Locate every blood parasite and identify its species.
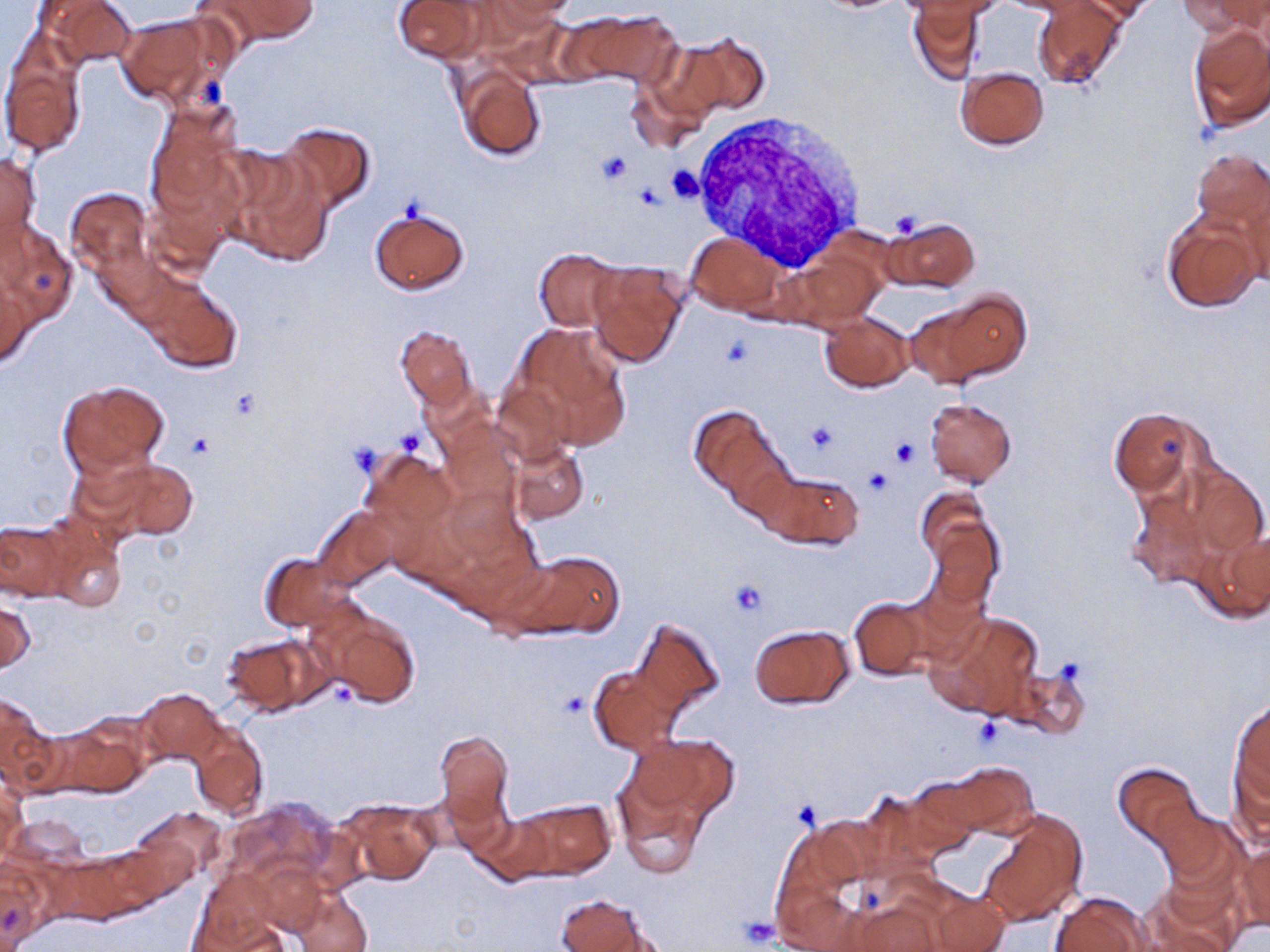
No blood parasites seen.

slide-level diagnosis = no evidence of blood parasites
platelet locations = approximate bounding boxes as (x1,y1)-(x2,y2) corner pairs in pixels: (596,152)-(632,186), (667,165)-(705,203), (885,209)-(927,239), (805,420)-(841,455), (395,429)-(425,454), (188,432)-(215,461), (890,438)-(921,468), (348,441)-(383,475), (864,467)-(893,495), (727,579)-(768,617), (557,690)-(589,717), (972,715)-(1005,748), (789,797)-(825,829), (735,917)-(779,947)
modality = light microscopy
magnification = 1000x
stain = May-Grünwald-Giemsa
uninfected red blood cell locations = approximate bounding boxes as (x1,y1)-(x2,y2) corner pairs in pixels: (40,0)-(139,68), (212,0)-(319,43), (392,0)-(480,62), (489,0)-(581,24), (917,0)-(1002,21), (1085,0)-(1160,24), (1180,0)-(1266,36), (1001,1)-(1085,14), (1034,2)-(1126,89), (910,5)-(985,84), (572,9)-(682,87), (118,14)-(220,107), (1188,22)-(1270,131), (682,33)-(770,117), (1,38)-(88,158), (456,65)-(546,161), (956,67)-(1048,150), (144,104)-(240,221), (277,120)-(376,211), (1190,147)-(1270,238), (0,151)-(41,252), (227,155)-(334,267), (1229,178)-(1270,284), (64,187)-(154,282), (370,206)-(470,295), (1161,211)-(1264,312), (885,216)-(980,292), (0,221)-(80,327), (688,234)-(782,315), (535,248)-(624,332), (791,248)-(886,330), (586,260)-(690,368), (140,274)-(243,372), (0,276)-(34,368), (916,295)-(1028,384), (819,313)-(914,392), (511,324)-(632,446), (395,325)-(477,409), (58,380)-(169,477), (925,397)-(1018,488), (689,405)-(785,502), (1111,406)-(1213,505), (509,442)-(589,523), (361,450)-(455,541), (90,455)-(198,543), (1174,461)-(1270,582), (759,469)-(864,549), (918,486)-(1001,603), (313,507)-(400,590), (39,515)-(129,613), (0,521)-(70,600), (1192,525)-(1270,624), (507,548)-(625,638), (259,552)-(354,633), (848,596)-(934,680), (1,598)-(35,676), (318,609)-(421,708), (927,610)-(1044,722), (632,617)-(725,713), (748,624)-(855,709), (222,632)-(328,715), (589,664)-(682,756), (1014,665)-(1091,739), (139,688)-(224,764), (0,694)-(55,790), (1229,698)-(1270,810), (56,717)-(152,799), (190,725)-(269,819), (435,729)-(515,835), (625,731)-(737,827), (934,760)-(1040,840), (1113,762)-(1201,845), (1,779)-(26,858), (617,787)-(707,879), (335,797)-(440,887), (223,798)-(342,889), (514,798)-(615,880), (1151,801)-(1238,887), (136,808)-(228,878), (980,809)-(1087,925), (472,813)-(558,886), (770,824)-(868,946), (1235,841)-(1269,932), (0,860)-(45,949), (190,876)-(292,952), (1142,881)-(1241,952), (923,887)-(1009,951), (293,889)-(372,952), (1051,891)-(1152,952), (554,893)-(658,952), (841,900)-(945,952)
field of view = one of a larger specimen
preparation = thin blood film
white blood cell locations = approximate bounding boxes as (x1,y1)-(x2,y2) corner pairs in pixels: (693,111)-(870,272)
image size = 1270×952 pixels